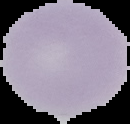
Summary:
  - Malaria status: uninfected
  - Preparation: thin blood smear
  - Image size: 130×124 pixels
  - Image type: cell region segmented out of the field of view; surrounding area masked to black